Classify this cell by malaria status.
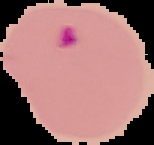
It is parasitized.

image type = segmented cell region with the area outside set to black
preparation = thin blood smear
image size = 154×145 pixels